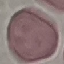
Summary:
  - Malaria status: uninfected
  - Image type: automatically extracted cell patch, resized to 64 × 64 pixels
  - Stain: Giemsa
  - Capture: smartphone through the microscope eyepiece
  - Preparation: thin blood film